State the blood parasite species.
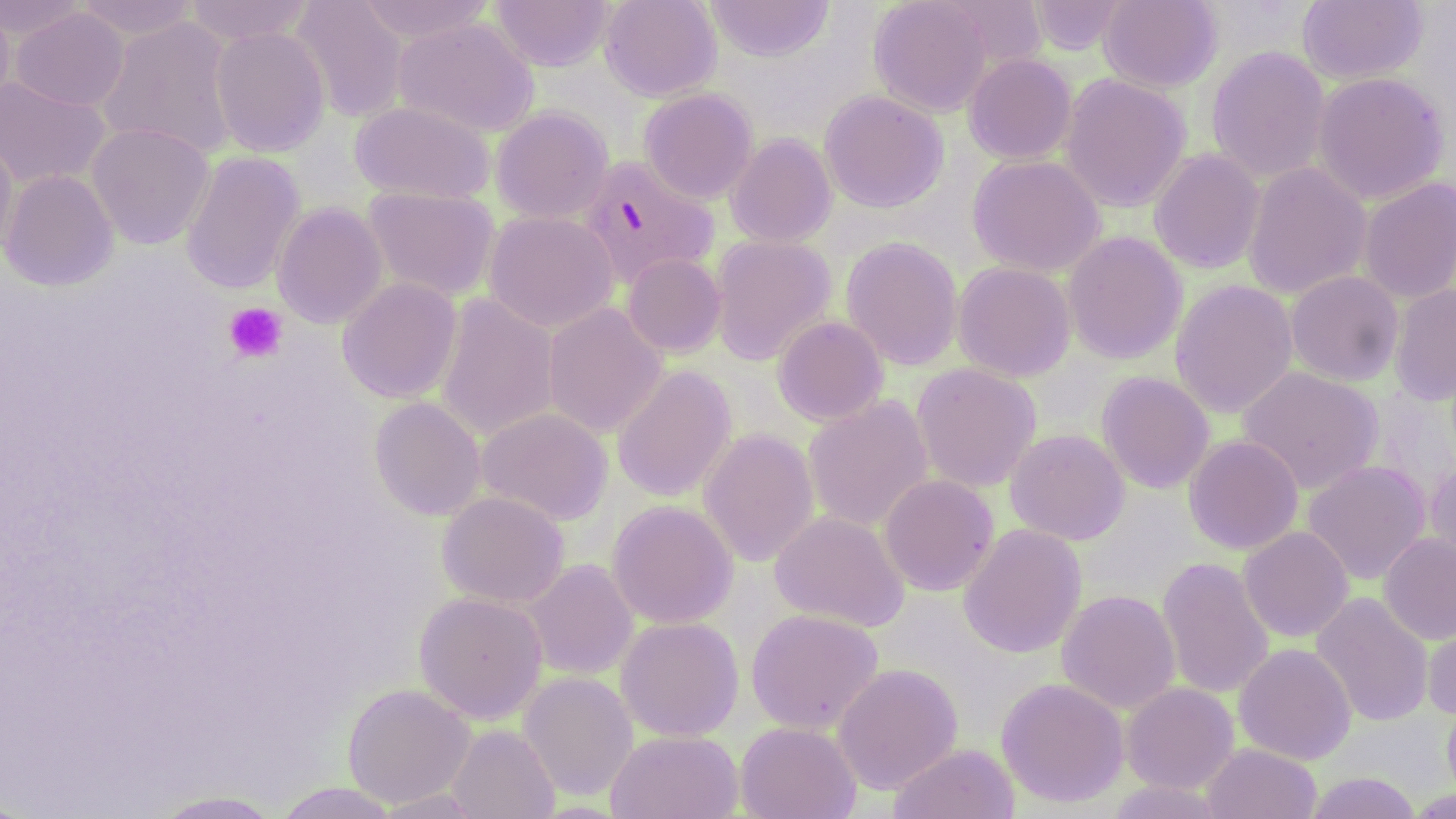
Plasmodium falciparum.

Approximate bounding boxes as (x1, y1, x2, y2) in pixels. Uninfected red blood cell locations: (0, 0, 88, 42), (73, 0, 201, 41), (182, 0, 316, 46), (291, 0, 408, 122), (353, 0, 497, 44), (599, 0, 722, 101), (704, 0, 835, 63), (868, 0, 994, 117), (1028, 0, 1130, 55), (1098, 0, 1222, 92), (1297, 0, 1427, 84), (490, 1, 615, 72), (0, 4, 16, 113), (9, 7, 129, 111), (97, 16, 241, 159), (392, 17, 539, 137), (209, 26, 331, 157), (1206, 46, 1330, 182), (963, 54, 1077, 164), (1312, 71, 1449, 205), (1059, 73, 1192, 212), (0, 75, 111, 190), (638, 88, 758, 204), (819, 90, 949, 213), (351, 101, 495, 203), (490, 106, 613, 224), (86, 122, 215, 249), (0, 132, 19, 261), (726, 134, 837, 247), (1149, 148, 1266, 274), (180, 151, 305, 295), (966, 154, 1105, 277), (1242, 162, 1372, 299), (1, 169, 120, 291), (1357, 177, 1456, 304), (362, 186, 501, 302), (272, 202, 388, 329), (483, 210, 619, 332), (1062, 231, 1187, 365), (710, 234, 837, 365), (840, 236, 963, 371), (622, 253, 727, 357), (952, 262, 1076, 381), (1286, 271, 1404, 386), (337, 277, 462, 404), (1170, 279, 1298, 418), (1389, 284, 1456, 406), (434, 293, 560, 442), (542, 302, 667, 438), (772, 315, 889, 426), (911, 363, 1042, 492), (611, 364, 737, 502), (1237, 366, 1383, 494), (1096, 371, 1215, 493), (369, 396, 486, 521), (802, 396, 934, 532), (475, 407, 613, 525), (698, 427, 819, 567), (1005, 428, 1130, 545), (1184, 434, 1304, 554), (1302, 460, 1431, 585), (1425, 461, 1456, 576), (878, 474, 999, 595), (437, 491, 569, 608), (607, 499, 738, 629), (769, 511, 909, 632), (958, 523, 1087, 658), (1239, 526, 1354, 642), (1378, 533, 1456, 644), (1156, 557, 1274, 700), (523, 559, 638, 680), (1057, 589, 1181, 714), (414, 591, 548, 723), (1310, 592, 1434, 728), (746, 608, 884, 734), (1422, 612, 1456, 720), (616, 616, 744, 741), (1234, 642, 1357, 764), (832, 663, 963, 794), (518, 671, 638, 801), (996, 677, 1129, 808), (1121, 682, 1239, 794), (342, 683, 475, 808), (1441, 696, 1456, 805), (735, 721, 861, 819), (446, 724, 559, 819), (606, 729, 743, 819), (888, 743, 1019, 819), (1201, 743, 1322, 819), (1303, 771, 1422, 818), (1103, 780, 1229, 819), (273, 782, 403, 818), (1405, 786, 1455, 817), (372, 788, 489, 818), (147, 790, 288, 818). Platelet locations: (224, 302, 288, 363). Plasmodium falciparum-infected red blood cell locations: (577, 154, 719, 288). Light microscopy. Thin blood smear. Image is 1456×819 pixels. One field of a larger specimen. Captured at 1000x magnification. May-Grünwald-Giemsa stain.